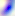
Summary:
  - Identification: Toxoplasma gondii
  - Modality: photomicrograph
  - Magnification: 400x